Mark where platelets are.
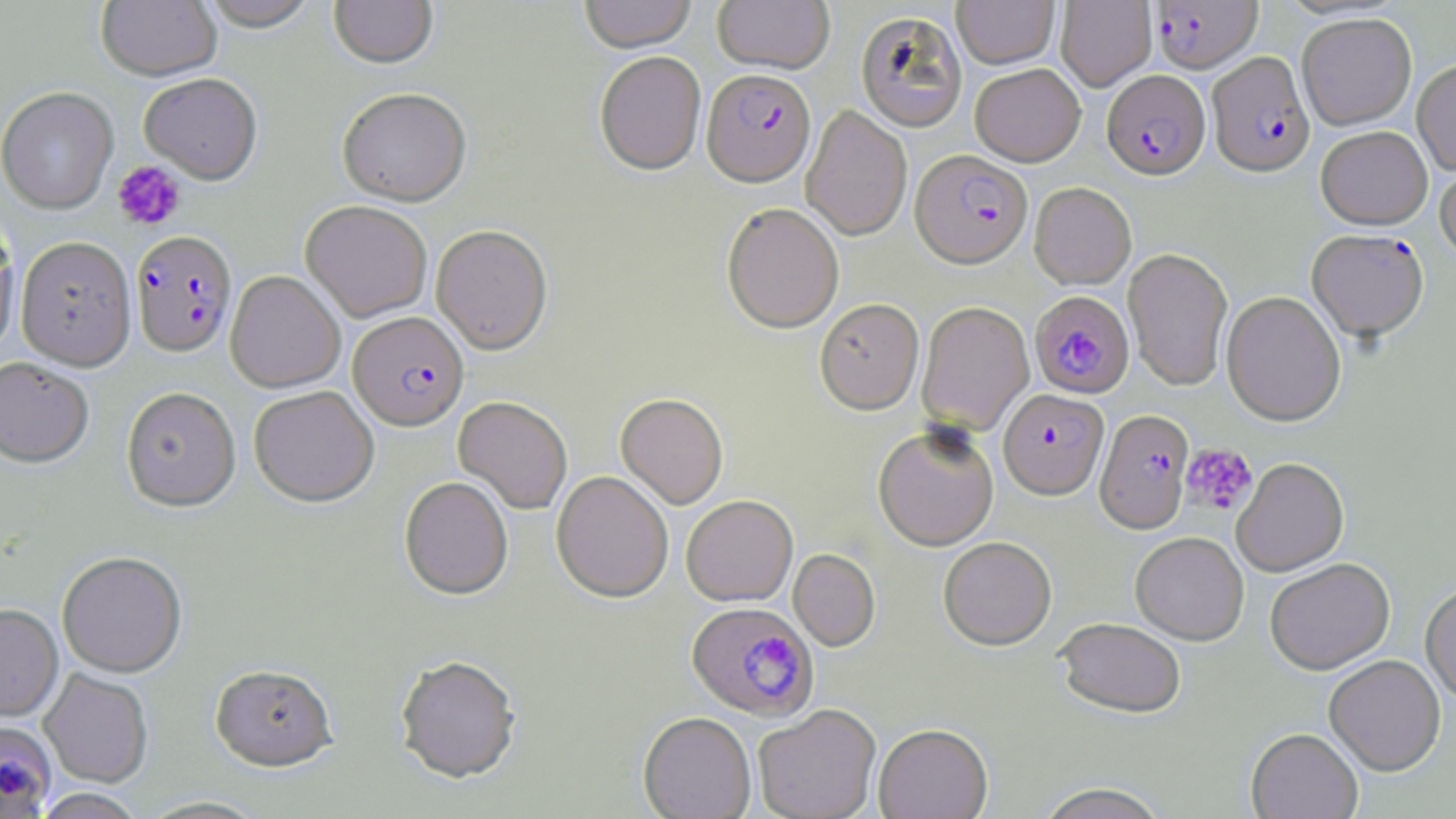

Approximate bounding boxes as named x1/y1/x2/y2 corners in pixels.
Platelets: (x1=113, y1=161, x2=186, y2=231), (x1=1181, y1=443, x2=1258, y2=517).

Uninfected red blood cell locations (subset): (x1=96, y1=0, x2=222, y2=84), (x1=199, y1=0, x2=320, y2=34), (x1=329, y1=0, x2=438, y2=71), (x1=580, y1=0, x2=696, y2=56), (x1=713, y1=0, x2=835, y2=76), (x1=952, y1=0, x2=1059, y2=70), (x1=1055, y1=0, x2=1156, y2=91), (x1=856, y1=12, x2=967, y2=133), (x1=1297, y1=14, x2=1417, y2=130), (x1=594, y1=54, x2=706, y2=179), (x1=1412, y1=60, x2=1456, y2=177), (x1=970, y1=65, x2=1085, y2=168), (x1=139, y1=75, x2=262, y2=185), (x1=0, y1=88, x2=118, y2=216), (x1=337, y1=91, x2=472, y2=208), (x1=801, y1=106, x2=912, y2=243), (x1=1316, y1=126, x2=1433, y2=230), (x1=1435, y1=158, x2=1456, y2=264), (x1=1029, y1=184, x2=1136, y2=290), (x1=300, y1=201, x2=432, y2=323), (x1=721, y1=205, x2=844, y2=336), (x1=0, y1=219, x2=19, y2=359), (x1=431, y1=226, x2=553, y2=356), (x1=17, y1=237, x2=136, y2=371), (x1=1123, y1=249, x2=1233, y2=392), (x1=1221, y1=291, x2=1346, y2=428), (x1=815, y1=300, x2=924, y2=416), (x1=917, y1=303, x2=1034, y2=436), (x1=0, y1=359, x2=94, y2=470), (x1=249, y1=386, x2=379, y2=508), (x1=121, y1=388, x2=241, y2=514), (x1=615, y1=394, x2=728, y2=511), (x1=453, y1=397, x2=573, y2=514), (x1=873, y1=426, x2=999, y2=552), (x1=1231, y1=459, x2=1349, y2=578), (x1=551, y1=472, x2=673, y2=604), (x1=399, y1=478, x2=513, y2=601), (x1=681, y1=495, x2=798, y2=608), (x1=1131, y1=534, x2=1248, y2=647), (x1=938, y1=539, x2=1057, y2=652), (x1=788, y1=549, x2=880, y2=652), (x1=57, y1=554, x2=187, y2=678), (x1=1265, y1=561, x2=1395, y2=676), (x1=1420, y1=584, x2=1456, y2=705), (x1=0, y1=605, x2=63, y2=724), (x1=1055, y1=620, x2=1187, y2=721), (x1=394, y1=656, x2=522, y2=786), (x1=1324, y1=656, x2=1446, y2=776), (x1=210, y1=666, x2=339, y2=774), (x1=40, y1=670, x2=153, y2=789), (x1=753, y1=706, x2=881, y2=819), (x1=638, y1=713, x2=756, y2=819), (x1=873, y1=726, x2=993, y2=819), (x1=1246, y1=729, x2=1362, y2=819), (x1=1035, y1=782, x2=1170, y2=819), (x1=32, y1=789, x2=148, y2=819), (x1=136, y1=796, x2=272, y2=819). Plasmodium falciparum-infected red blood cell locations (subset): (x1=1151, y1=0, x2=1262, y2=75), (x1=1207, y1=53, x2=1315, y2=179), (x1=1101, y1=71, x2=1211, y2=183), (x1=701, y1=72, x2=816, y2=191), (x1=910, y1=152, x2=1033, y2=271), (x1=1307, y1=230, x2=1430, y2=344), (x1=131, y1=231, x2=238, y2=359), (x1=1029, y1=292, x2=1134, y2=401), (x1=348, y1=313, x2=469, y2=432), (x1=998, y1=390, x2=1110, y2=503), (x1=1095, y1=410, x2=1193, y2=536), (x1=686, y1=604, x2=819, y2=723), (x1=0, y1=722, x2=57, y2=818). Slide-level diagnosis: Plasmodium falciparum. May-Grünwald-Giemsa stain. Thin blood film. 1000x magnification. Optical microscopy. One field of a larger specimen. Image is 1456×819 pixels.